Classify this cell by malaria status.
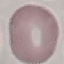

Uninfected.

preparation: thin smear
stain: Giemsa
capture: smartphone camera at the microscope eyepiece
image_type: cell patch, automatically extracted from a larger field of view and resized to 64 × 64 pixels